Report the malaria status of this cell.
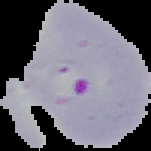

Parasitized.

Summary:
  - Image size: 151×151 pixels
  - Image type: cell region segmented out of the field of view; surrounding area masked to black
  - Preparation: thin blood film